Assess this cell for malaria.
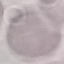
Uninfected.

Summary:
  - Preparation: thin blood smear
  - Image type: automatically extracted cell patch, resized to 64 × 64 pixels
  - Stain: Giemsa
  - Capture: smartphone through the microscope eyepiece